Assess this cell for malaria.
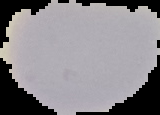
It is uninfected.

Segmented cell region on a black background. From a thin blood smear. Image is 160×115 pixels.